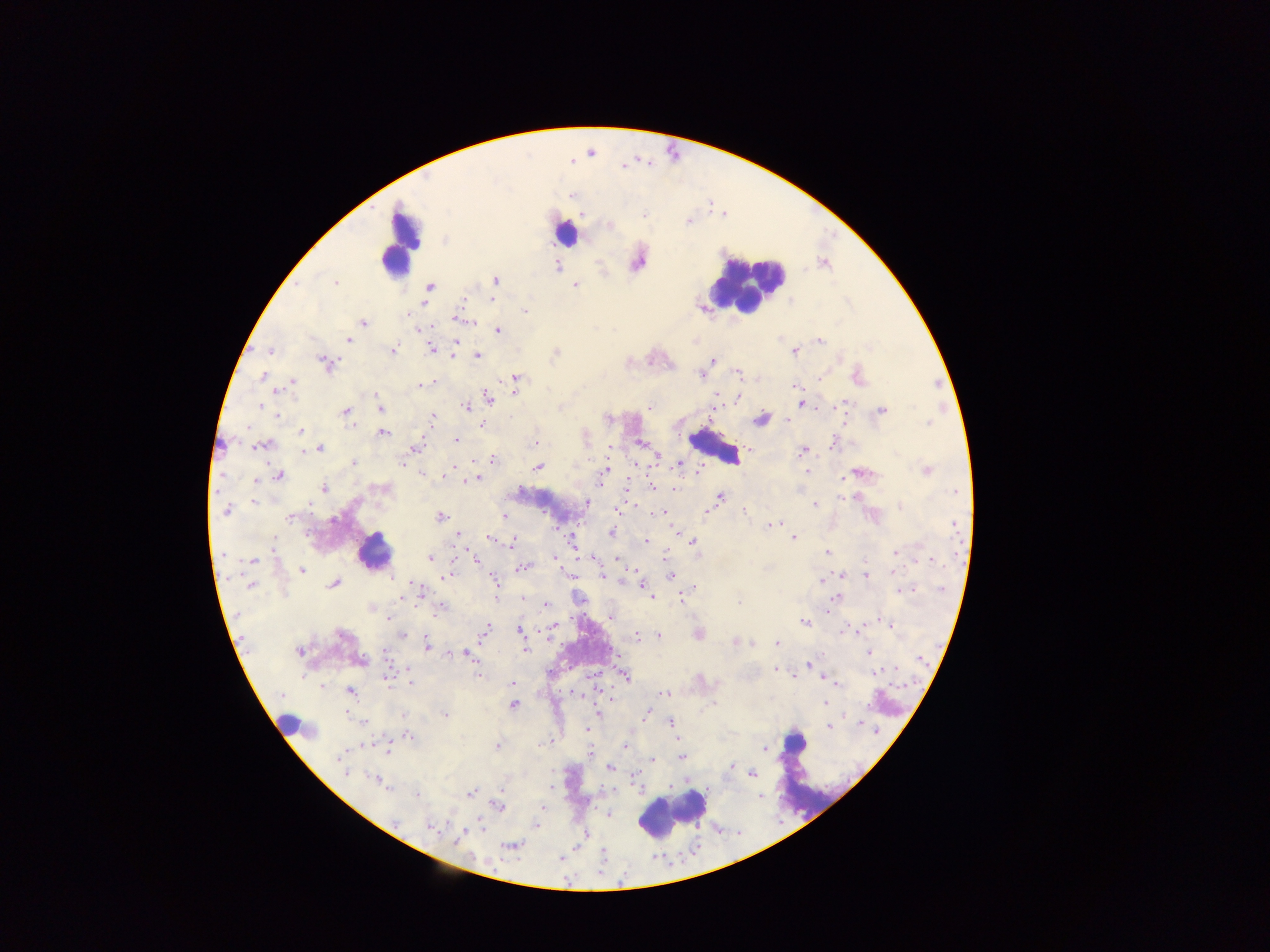 Approximate centers as {x, y} in pixels. Leukocyte locations: {566, 233}, {400, 259}, {751, 277}, {375, 547}, {673, 813}. Malaria parasite locations: {446, 241}, {639, 264}, {557, 267}, {496, 279}, {335, 282}, {575, 285}, {428, 287}, {461, 299}, {493, 300}, {424, 306}, {526, 312}, {705, 316}, {363, 321}, {497, 329}, {348, 339}, {456, 340}, {694, 341}, {820, 341}, {430, 347}, {270, 351}, {392, 351}, {456, 352}, {796, 353}, {478, 355}, {712, 359}, {628, 363}, {325, 364}, {737, 373}, {700, 375}, {263, 378}, {514, 379}, {292, 383}, {422, 384}, {416, 385}, {514, 386}, {796, 386}, {276, 391}, {513, 393}, {719, 395}, {737, 396}, {487, 397}, {294, 401}, {801, 404}, {257, 407}, {649, 407}, {381, 408}, {881, 408}, {465, 409}, {645, 409}, {345, 411}, {278, 417}, {762, 418}, {432, 419}, {788, 419}, {928, 423}, {354, 424}, {480, 424}, {251, 427}, {302, 432}, {384, 434}, {456, 440}, {533, 442}, {640, 444}, {262, 446}, {321, 448}, {417, 449}, {802, 449}, {304, 452}, {658, 456}, {493, 459}, {400, 462}, {353, 464}, {679, 464}, {538, 468}, {605, 470}, {926, 470}, {806, 471}, {423, 473}, {280, 475}, {478, 477}, {257, 483}, {323, 487}, {651, 487}, {675, 488}, {720, 497}, {841, 499}, {254, 504}, {589, 504}, {814, 504}, {901, 508}, {225, 511}, {616, 511}, {745, 512}, {659, 513}, {706, 513}, {503, 516}, {440, 517}, {289, 518}, {776, 522}, {770, 526}, {611, 532}, {676, 532}, {457, 536}, {794, 537}, {487, 538}, {512, 542}, {644, 542}, {692, 543}, {826, 552}, {895, 552}, {221, 554}, {472, 556}, {553, 557}, {432, 558}, {594, 559}, {917, 559}, {475, 560}, {556, 560}, {255, 561}, {525, 567}, {302, 570}, {637, 571}, {866, 575}, {446, 576}, {569, 576}, {603, 576}, {669, 577}, {495, 581}, {822, 581}, {334, 583}, {625, 583}, {642, 583}, {251, 584}, {911, 590}, {418, 591}, {902, 591}, {421, 594}, {522, 597}, {400, 598}, {681, 598}, {837, 598}, {652, 599}, {497, 600}, {739, 601}, {546, 606}, {440, 612}, {437, 614}, {237, 615}, {388, 619}, {804, 623}, {893, 624}, {554, 625}, {486, 628}, {518, 629}, {553, 632}, {486, 633}, {402, 635}, {638, 635}, {659, 635}, {733, 641}, {775, 643}, {752, 644}, {427, 647}, {527, 648}, {300, 653}, {867, 653}, {466, 654}, {385, 659}, {471, 659}, {808, 663}, {774, 670}, {876, 672}, {303, 674}, {385, 675}, {477, 676}, {627, 676}, {409, 678}, {833, 683}, {319, 684}, {511, 684}, {837, 686}, {322, 687}, {349, 692}, {664, 693}, {514, 705}, {825, 706}, {646, 714}, {445, 715}, {404, 716}, {849, 716}, {670, 723}, {828, 727}, {587, 728}, {879, 732}, {409, 737}, {678, 740}, {497, 746}, {624, 746}, {768, 749}, {387, 750}, {591, 751}, {337, 756}, {679, 758}, {653, 760}, {731, 767}, {609, 768}, {344, 772}, {752, 773}, {375, 781}, {471, 793}, {416, 795}, {757, 797}, {606, 814}, {428, 824}, {460, 834}, {586, 835}, {509, 847}. Thick blood smear. Collected in Ghana. Photographed through a microscope with a mobile-phone camera. Image is 1270×952 pixels. One field of view.